Classify this cell by malaria status.
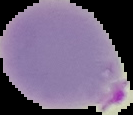
Parasitized.

Image is 133×115 pixels. Cell region segmented out of the field of view; the surrounding area is masked to black. From a thin blood smear.